Classify this cell by malaria status.
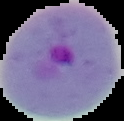

Parasitized.

Summary:
  - Preparation: thin blood film
  - Image type: segmented cell region on a black background
  - Image size: 124×121 pixels